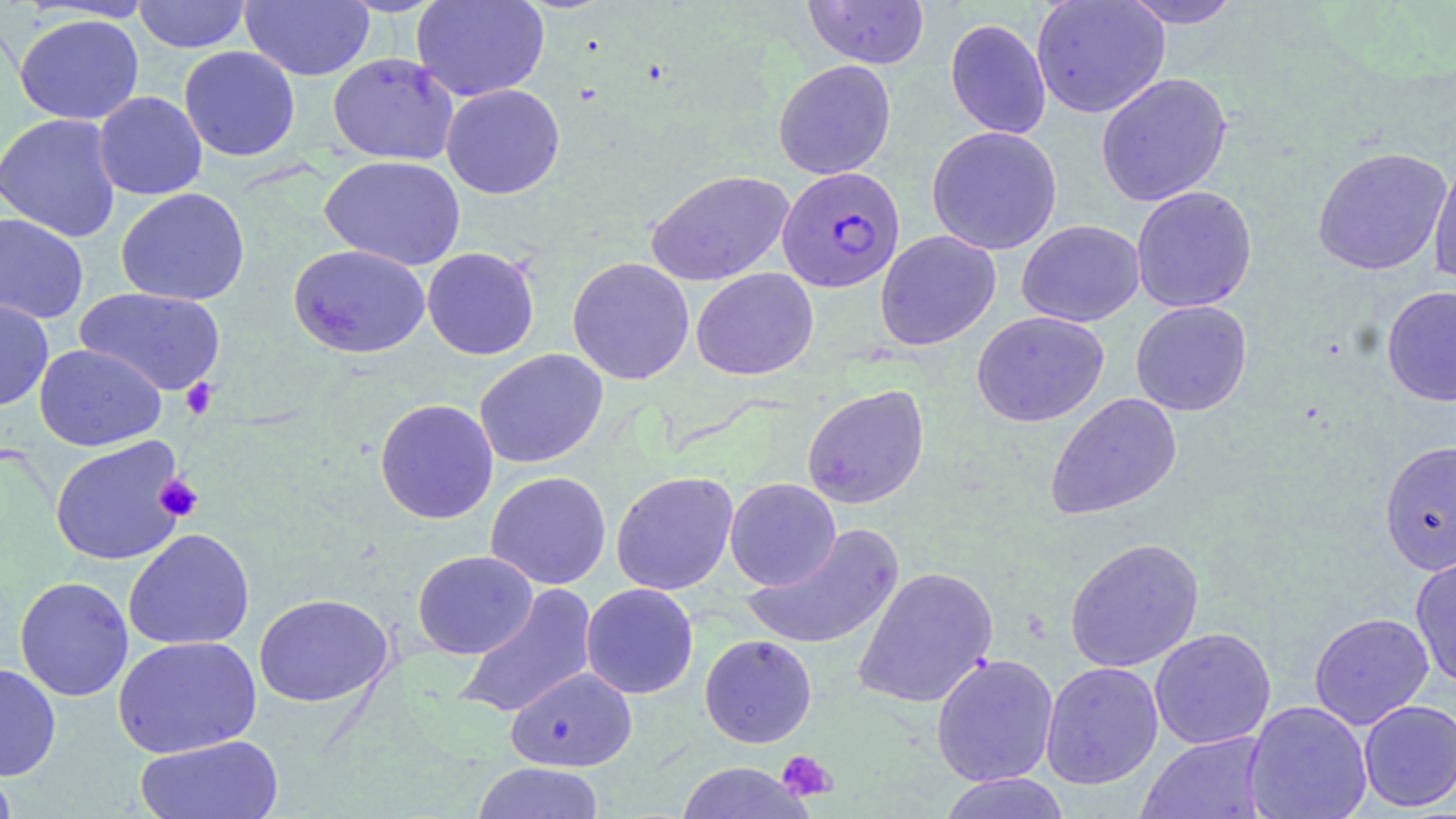

Approximate bounding boxes as named x1/y1/x2/y2 corners in pixels. Plasmodium falciparum-infected red blood cell locations: (x1=777, y1=166, x2=905, y2=293). Uninfected red blood cell locations: (x1=133, y1=0, x2=251, y2=53), (x1=240, y1=0, x2=375, y2=81), (x1=411, y1=0, x2=549, y2=102), (x1=802, y1=0, x2=929, y2=69), (x1=1031, y1=0, x2=1170, y2=118), (x1=1119, y1=0, x2=1245, y2=29), (x1=13, y1=13, x2=145, y2=125), (x1=945, y1=18, x2=1051, y2=139), (x1=178, y1=45, x2=300, y2=162), (x1=328, y1=53, x2=459, y2=165), (x1=773, y1=59, x2=896, y2=180), (x1=1095, y1=72, x2=1233, y2=207), (x1=441, y1=83, x2=565, y2=199), (x1=93, y1=91, x2=208, y2=200), (x1=0, y1=112, x2=123, y2=242), (x1=926, y1=125, x2=1063, y2=255), (x1=1312, y1=146, x2=1453, y2=276), (x1=1428, y1=153, x2=1456, y2=290), (x1=319, y1=155, x2=467, y2=270), (x1=645, y1=169, x2=794, y2=286), (x1=1131, y1=185, x2=1257, y2=313), (x1=116, y1=188, x2=250, y2=306), (x1=0, y1=213, x2=89, y2=324), (x1=1016, y1=219, x2=1145, y2=327), (x1=875, y1=230, x2=1001, y2=351), (x1=288, y1=244, x2=431, y2=359), (x1=422, y1=247, x2=539, y2=360), (x1=567, y1=256, x2=694, y2=385), (x1=691, y1=267, x2=818, y2=380), (x1=1381, y1=285, x2=1456, y2=407), (x1=75, y1=287, x2=226, y2=396), (x1=0, y1=298, x2=54, y2=411), (x1=1130, y1=300, x2=1252, y2=416), (x1=971, y1=310, x2=1109, y2=428), (x1=34, y1=343, x2=166, y2=451), (x1=474, y1=348, x2=609, y2=469), (x1=801, y1=384, x2=930, y2=509), (x1=1045, y1=392, x2=1183, y2=520), (x1=374, y1=398, x2=499, y2=525), (x1=50, y1=436, x2=187, y2=566), (x1=1379, y1=439, x2=1456, y2=575), (x1=485, y1=471, x2=612, y2=590), (x1=611, y1=471, x2=739, y2=595), (x1=724, y1=477, x2=841, y2=590), (x1=740, y1=523, x2=906, y2=651), (x1=123, y1=528, x2=255, y2=651), (x1=1064, y1=537, x2=1204, y2=672), (x1=412, y1=550, x2=538, y2=659), (x1=1410, y1=551, x2=1456, y2=689), (x1=853, y1=565, x2=998, y2=709), (x1=15, y1=576, x2=134, y2=702), (x1=580, y1=583, x2=699, y2=699), (x1=455, y1=584, x2=598, y2=720), (x1=253, y1=593, x2=394, y2=707), (x1=1308, y1=611, x2=1434, y2=730), (x1=1150, y1=627, x2=1276, y2=750), (x1=699, y1=634, x2=817, y2=748), (x1=112, y1=635, x2=262, y2=758), (x1=930, y1=653, x2=1059, y2=788), (x1=1041, y1=661, x2=1164, y2=790), (x1=0, y1=662, x2=61, y2=781), (x1=505, y1=666, x2=637, y2=772), (x1=1358, y1=699, x2=1456, y2=811), (x1=1243, y1=700, x2=1373, y2=819), (x1=1136, y1=731, x2=1272, y2=819), (x1=135, y1=734, x2=285, y2=819), (x1=471, y1=761, x2=606, y2=819), (x1=674, y1=762, x2=813, y2=818), (x1=0, y1=766, x2=19, y2=818), (x1=937, y1=772, x2=1072, y2=819). Platelet locations: (x1=180, y1=378, x2=219, y2=420), (x1=154, y1=474, x2=204, y2=523), (x1=776, y1=750, x2=837, y2=801). Slide-level diagnosis: Plasmodium falciparum. Thin blood film. Image is 1456×819 pixels. One field of a larger specimen. Light microscopy. 1000x magnification. May-Grünwald-Giemsa-stained preparation.